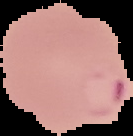

preparation = thin blood film
image type = segmented cell region with the area outside set to black
image size = 133×136 pixels
malaria status = parasitized